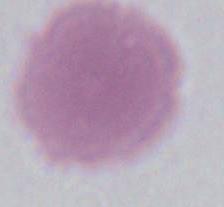
magnification = 1000x
modality = photomicrograph
identification = erythrocyte